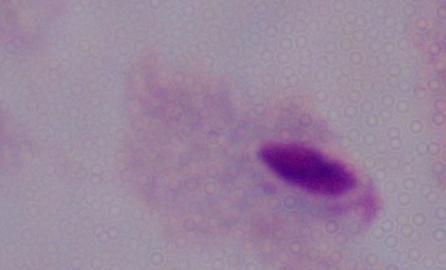
Summary:
  - Magnification: 1000x
  - Modality: micrograph
  - Identification: trichomonad